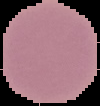

preparation: thin blood smear
image_size: 100×106 pixels
image_type: segmented cell region on a black background
malaria_status: uninfected